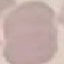
Result: no malaria parasites detected. Giemsa-stained preparation. Thin blood smear. Photographed with a smartphone camera at the microscope eyepiece. Automatically extracted cell patch, resized to 64 × 64 pixels.